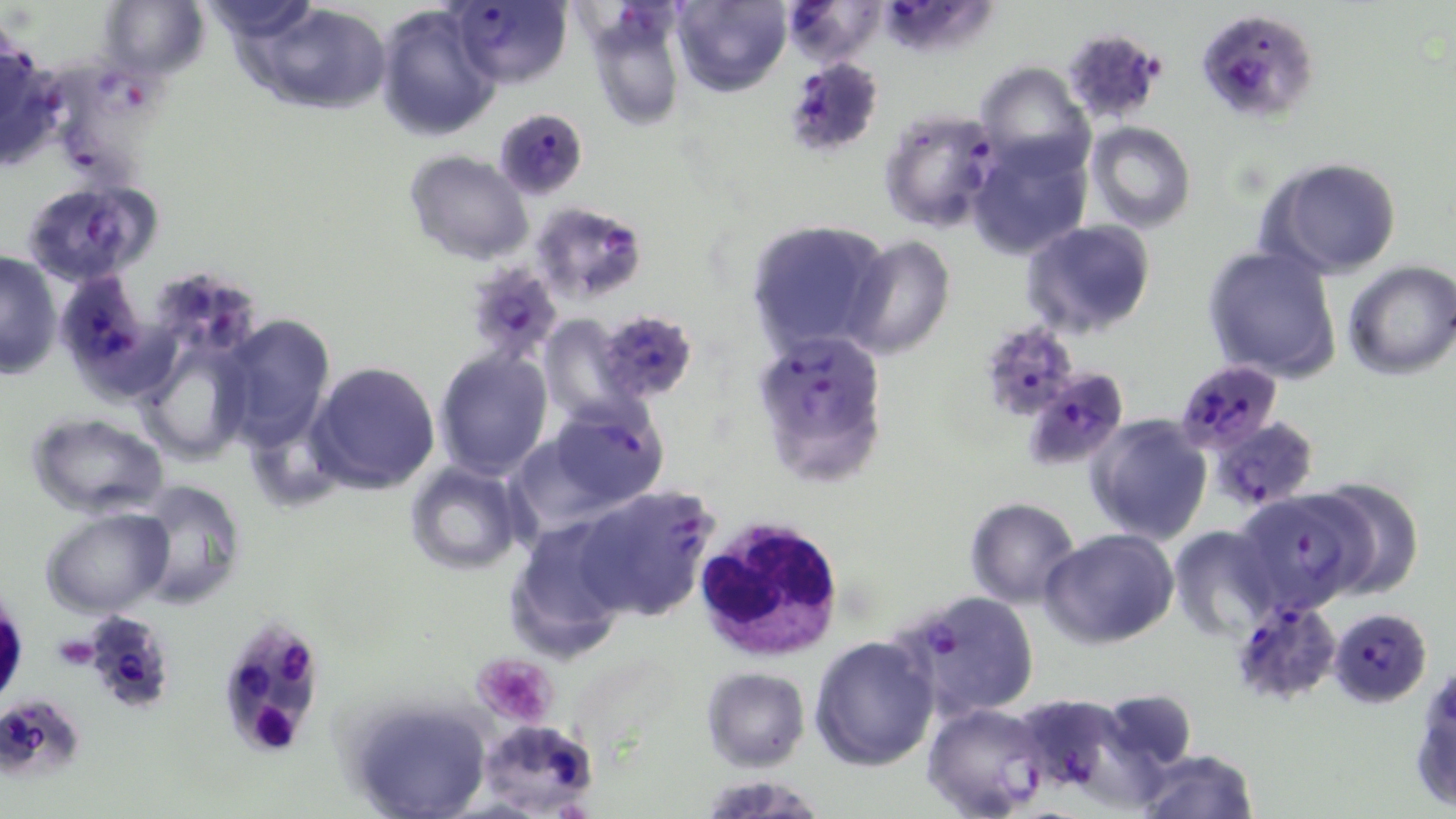
slide-level diagnosis = Plasmodium falciparum
uninfected red blood cell locations = approximate bounding boxes as (x1,y1)-(x2,y2) corner pairs in pixels: (99,0)-(210,80), (204,0)-(321,52), (672,0)-(792,97), (247,3)-(392,115), (375,6)-(500,142), (584,8)-(687,131), (975,61)-(1094,177), (1086,122)-(1197,233), (966,137)-(1092,260), (404,149)-(535,265), (1260,157)-(1402,279), (746,218)-(891,356), (1023,220)-(1157,339), (842,235)-(956,360), (1202,244)-(1342,383), (0,250)-(63,379), (1343,260)-(1456,381), (219,313)-(339,447), (538,314)-(639,426), (133,336)-(255,466), (433,347)-(554,481), (308,361)-(442,495), (26,411)-(169,520), (1086,415)-(1213,545), (405,462)-(525,576), (1308,477)-(1425,600), (129,480)-(247,609), (964,497)-(1081,609), (40,506)-(174,618), (505,520)-(632,659), (1169,526)-(1280,641), (1040,528)-(1179,650), (809,635)-(940,772), (701,666)-(811,772), (1410,672)-(1456,813), (346,698)-(493,819), (1136,749)-(1260,819), (696,774)-(830,818)
magnification = 1000x
stain = May-Grünwald-Giemsa
field of view = single
image size = 1456×819 pixels
Plasmodium falciparum-infected red blood cell locations = approximate bounding boxes as (x1,y1)-(x2,y2) corner pairs in pixels: (448,0)-(573,88), (781,0)-(888,67), (878,0)-(996,61), (1194,8)-(1321,125), (1060,28)-(1167,126), (0,34)-(62,170), (782,56)-(886,160), (42,58)-(161,196), (494,108)-(589,201), (877,108)-(1003,233), (22,178)-(162,288), (530,201)-(648,305), (461,262)-(565,366), (53,269)-(158,394), (154,273)-(257,356), (595,309)-(699,404), (978,321)-(1081,422), (753,327)-(890,479), (1173,360)-(1284,454), (1023,367)-(1130,470), (542,401)-(669,515), (1208,416)-(1320,511), (572,484)-(719,623), (1235,490)-(1371,614), (898,590)-(1041,720), (1230,598)-(1343,706), (1328,607)-(1432,707), (77,610)-(179,715), (216,618)-(326,755), (0,694)-(86,783), (1027,696)-(1119,788), (920,703)-(1050,819), (477,718)-(600,817)
modality = light microscopy
platelet locations = approximate bounding boxes as (x1,y1)-(x2,y2) corner pairs in pixels: (471,653)-(559,728)
preparation = thin blood smear
white blood cell locations = approximate bounding boxes as (x1,y1)-(x2,y2) corner pairs in pixels: (692,514)-(846,663)